Classify this cell by malaria status.
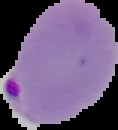
Parasitized.

image type = segmented cell region with the area outside set to black
image size = 118×130 pixels
preparation = thin blood film